Assess this cell for malaria.
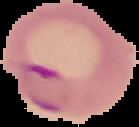
It is parasitized.

From a thin blood smear. Image is 139×127 pixels. Segmented cell region on a black background.